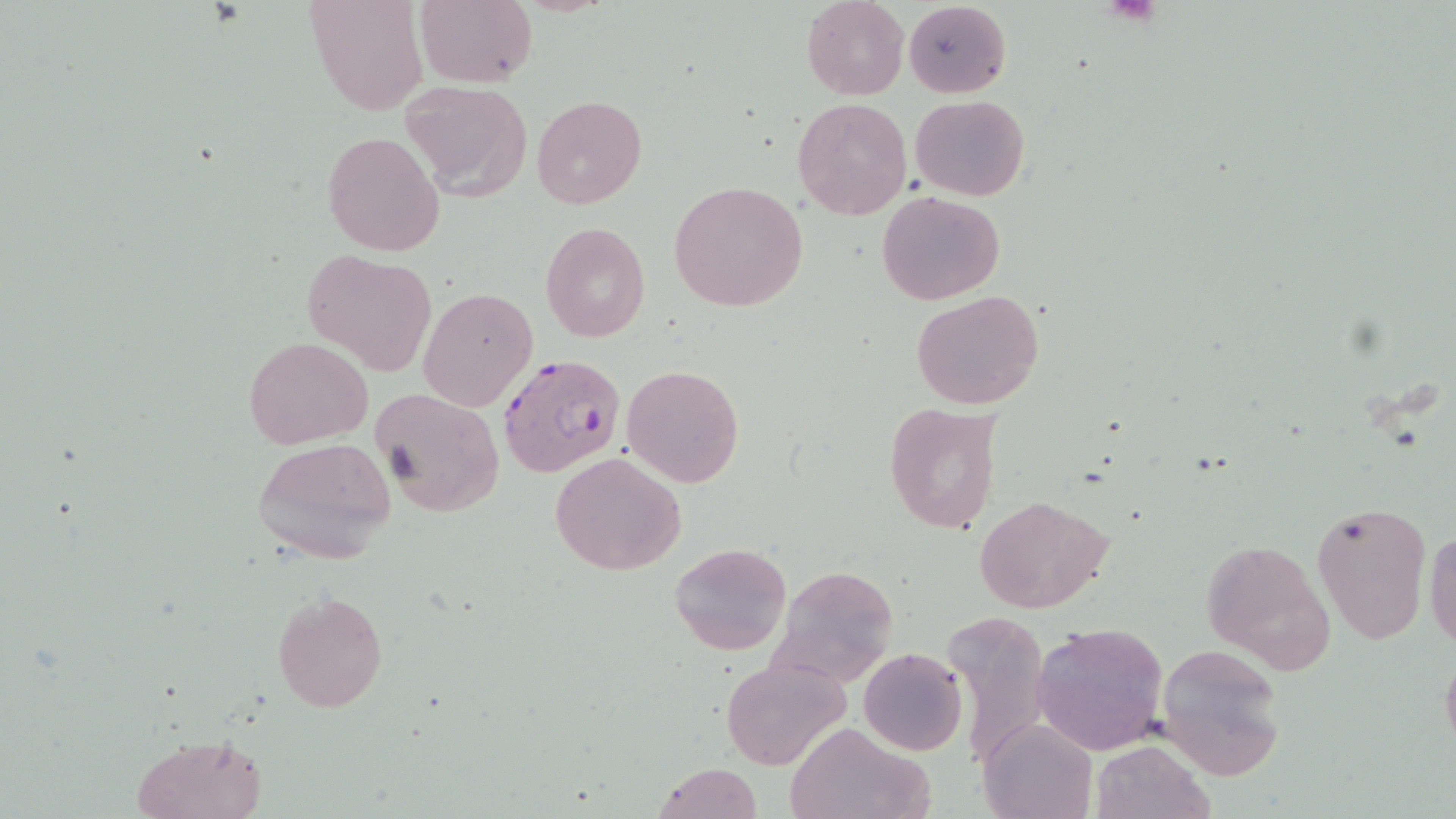
slide-level diagnosis = Plasmodium falciparum
magnification = 1000x
image size = 1456×819 pixels
stain = May-Grünwald-Giemsa
preparation = thin blood smear
uninfected red blood cell locations = approximate bounding boxes as (x1, y1, x2, y2) in pixels: (306, 0, 429, 117), (415, 0, 537, 88), (801, 0, 909, 100), (903, 2, 1012, 97), (396, 80, 532, 200), (531, 95, 647, 210), (911, 95, 1029, 201), (792, 97, 911, 219), (322, 130, 445, 256), (669, 181, 808, 313), (876, 191, 1006, 305), (539, 222, 650, 343), (304, 249, 437, 377), (418, 286, 538, 412), (911, 290, 1045, 411), (244, 337, 372, 449), (622, 364, 744, 487), (370, 387, 505, 517), (883, 402, 1000, 534), (251, 437, 398, 565), (549, 451, 688, 576), (974, 494, 1116, 614), (1312, 500, 1432, 645), (1426, 523, 1456, 650), (1198, 539, 1332, 670), (670, 542, 791, 657), (769, 564, 900, 689), (272, 591, 387, 713), (942, 611, 1052, 769), (1033, 623, 1169, 754), (1155, 643, 1287, 780), (1440, 643, 1456, 760), (858, 648, 967, 756), (721, 656, 850, 771), (978, 717, 1095, 819), (783, 720, 930, 819), (131, 732, 268, 818), (1090, 740, 1211, 819), (650, 762, 763, 819)
field of view = single
modality = optical microscopy
Plasmodium falciparum-infected red blood cell locations = approximate bounding boxes as (x1, y1, x2, y2) in pixels: (498, 354, 626, 479)